Classify this cell by malaria status.
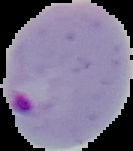

Parasitized.

From a thin blood film. Image is 133×151 pixels. The area outside the segmented cell region is set to black.